Mark where platelets are.
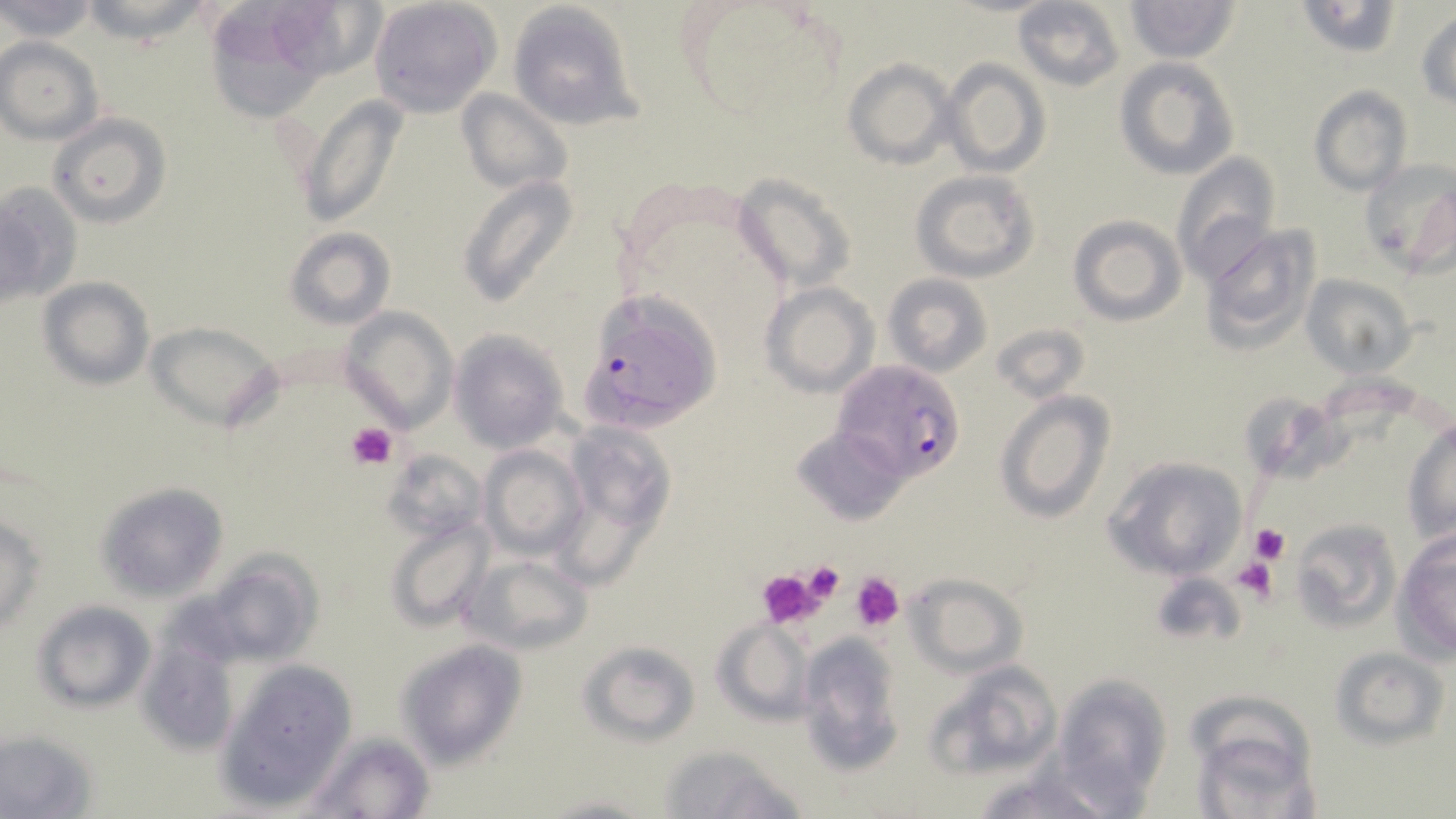

Approximate bounding boxes as named x1/y1/x2/y2 corners in pixels.
Platelets: (x1=346, y1=422, x2=395, y2=470), (x1=1249, y1=522, x2=1290, y2=564), (x1=1233, y1=558, x2=1280, y2=605), (x1=800, y1=560, x2=846, y2=605), (x1=754, y1=567, x2=828, y2=628), (x1=851, y1=572, x2=904, y2=632).

Uninfected red blood cell locations: (x1=0, y1=0, x2=99, y2=44), (x1=81, y1=0, x2=206, y2=45), (x1=367, y1=0, x2=501, y2=117), (x1=1012, y1=0, x2=1127, y2=91), (x1=1125, y1=0, x2=1240, y2=62), (x1=203, y1=1, x2=371, y2=109), (x1=1294, y1=1, x2=1404, y2=58), (x1=505, y1=2, x2=642, y2=131), (x1=1415, y1=9, x2=1456, y2=109), (x1=1, y1=36, x2=104, y2=145), (x1=1114, y1=57, x2=1238, y2=180), (x1=842, y1=58, x2=955, y2=170), (x1=941, y1=58, x2=1049, y2=176), (x1=1309, y1=86, x2=1412, y2=196), (x1=456, y1=88, x2=573, y2=198), (x1=293, y1=96, x2=409, y2=229), (x1=49, y1=113, x2=171, y2=228), (x1=1171, y1=152, x2=1280, y2=281), (x1=1358, y1=158, x2=1456, y2=275), (x1=911, y1=169, x2=1038, y2=280), (x1=732, y1=173, x2=854, y2=297), (x1=457, y1=174, x2=581, y2=309), (x1=0, y1=181, x2=80, y2=308), (x1=1067, y1=214, x2=1187, y2=326), (x1=1200, y1=223, x2=1324, y2=351), (x1=284, y1=228, x2=395, y2=329), (x1=882, y1=273, x2=992, y2=377), (x1=1301, y1=273, x2=1417, y2=376), (x1=39, y1=278, x2=154, y2=390), (x1=759, y1=282, x2=878, y2=397), (x1=338, y1=306, x2=459, y2=432), (x1=146, y1=321, x2=283, y2=431), (x1=991, y1=322, x2=1090, y2=404), (x1=448, y1=330, x2=568, y2=452), (x1=993, y1=389, x2=1116, y2=524), (x1=1248, y1=391, x2=1347, y2=473), (x1=1402, y1=417, x2=1455, y2=544), (x1=564, y1=421, x2=675, y2=534), (x1=794, y1=427, x2=907, y2=524), (x1=481, y1=446, x2=588, y2=561), (x1=383, y1=450, x2=485, y2=544), (x1=1101, y1=455, x2=1249, y2=582), (x1=97, y1=482, x2=228, y2=602), (x1=1, y1=513, x2=45, y2=633), (x1=384, y1=516, x2=491, y2=631), (x1=1289, y1=517, x2=1401, y2=633), (x1=1393, y1=530, x2=1456, y2=662), (x1=194, y1=551, x2=325, y2=666), (x1=464, y1=553, x2=594, y2=654), (x1=903, y1=574, x2=1028, y2=677), (x1=32, y1=601, x2=156, y2=712), (x1=711, y1=618, x2=816, y2=727), (x1=138, y1=632, x2=242, y2=756), (x1=797, y1=636, x2=906, y2=774), (x1=396, y1=640, x2=527, y2=767), (x1=579, y1=640, x2=700, y2=744), (x1=1331, y1=647, x2=1448, y2=748), (x1=218, y1=658, x2=359, y2=810), (x1=924, y1=659, x2=1064, y2=778), (x1=1053, y1=673, x2=1174, y2=813), (x1=1191, y1=720, x2=1318, y2=818), (x1=0, y1=729, x2=101, y2=818), (x1=306, y1=732, x2=436, y2=818), (x1=658, y1=746, x2=806, y2=819), (x1=971, y1=766, x2=1117, y2=818), (x1=536, y1=791, x2=657, y2=817). Plasmodium falciparum-infected red blood cell locations: (x1=578, y1=316, x2=716, y2=430), (x1=833, y1=361, x2=966, y2=483). Slide-level diagnosis: Plasmodium falciparum. Light microscopy. May-Grünwald-Giemsa stain. Single field of view. Thin blood smear. Image is 1456×819 pixels. 1000x magnification.